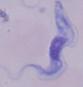
A trypanosome is seen. Photomicrograph. 1000x magnification.